Report the malaria status of this cell.
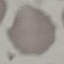
It is uninfected.

capture = smartphone through the microscope eyepiece
image type = automatically extracted cell patch, resized to 64 × 64 pixels
preparation = thin smear
stain = Giemsa